Identify the parasite.
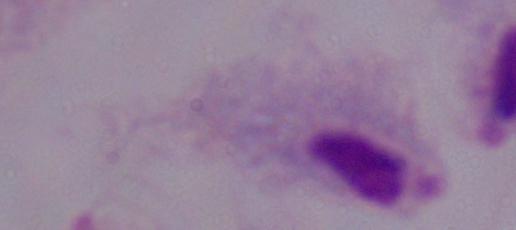
A trichomonad.

modality = photomicrograph
magnification = 1000x